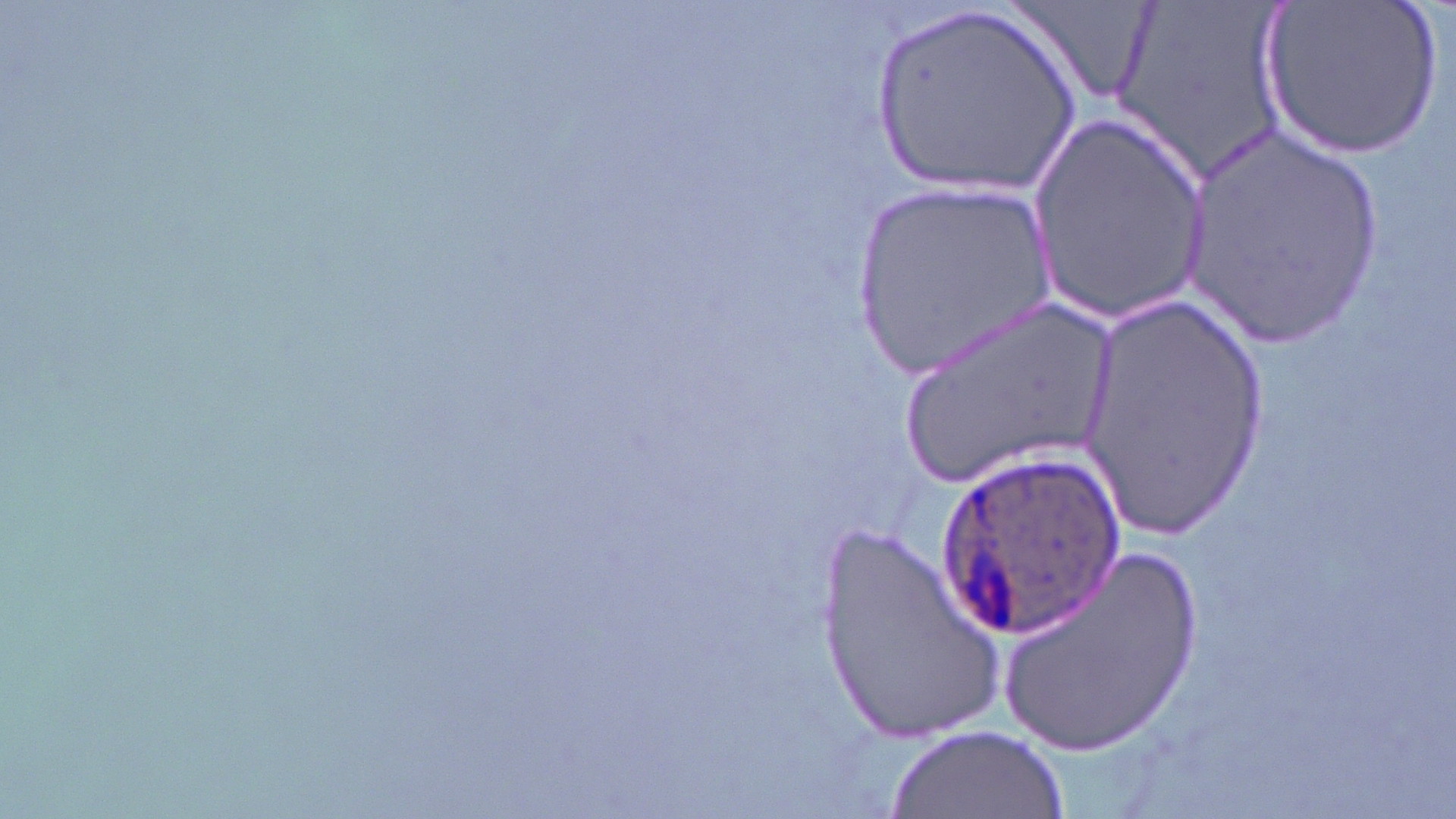
Summary:
  - Coordinate format: approximate bounding boxes as [x1, y1, x2, y2] in pixels
  - Uninfected red blood cell locations: [1005, 0, 1160, 108], [1112, 0, 1293, 185], [1257, 0, 1444, 162], [864, 3, 1084, 206], [1030, 112, 1212, 322], [1179, 130, 1391, 349], [851, 180, 1057, 389], [1074, 293, 1273, 534], [887, 295, 1133, 504], [815, 521, 1011, 745], [996, 540, 1207, 757], [887, 727, 1069, 819]
  - Plasmodium ovale-infected red blood cell locations: [933, 443, 1120, 643]
  - Slide-level diagnosis: Plasmodium ovale
  - Field of view: one of a larger specimen
  - Modality: optical microscopy
  - Magnification: 1000x
  - Stain: May-Grünwald-Giemsa
  - Image size: 1456×819 pixels
  - Preparation: thin blood smear